Give the extent of all uninfected red blood cells.
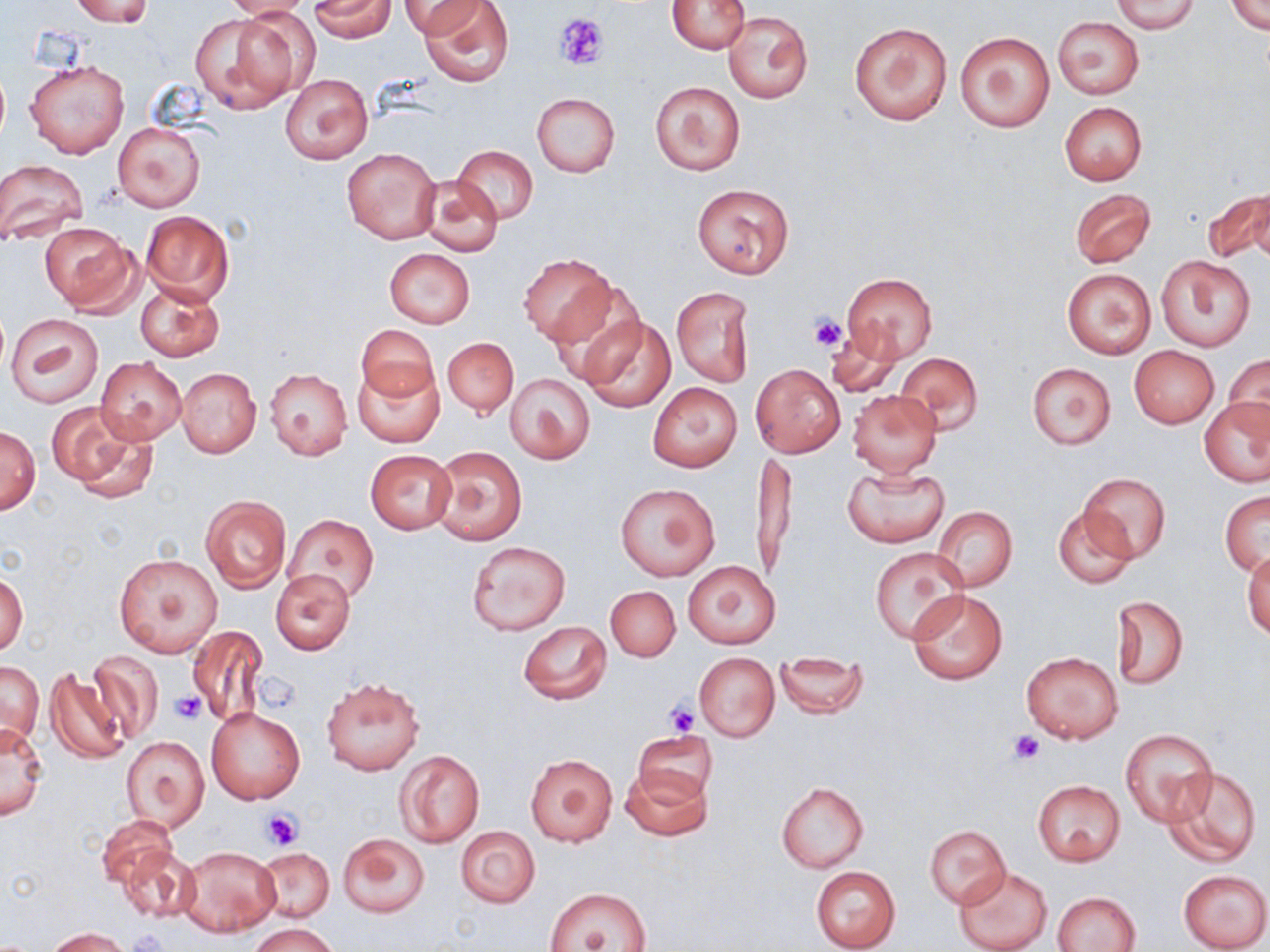

Approximate bounding boxes as (x1, y1, x2, y2) in pixels.
Uninfected red blood cells: (70, 0, 155, 26), (221, 0, 314, 20), (308, 0, 396, 41), (400, 0, 488, 38), (1111, 0, 1200, 33), (420, 1, 515, 87), (667, 1, 749, 53), (1227, 1, 1269, 35), (724, 11, 812, 104), (192, 13, 301, 113), (1052, 16, 1144, 99), (850, 23, 952, 126), (954, 31, 1057, 133), (25, 58, 129, 159), (281, 73, 372, 163), (650, 80, 745, 176), (531, 92, 620, 176), (1059, 101, 1146, 185), (113, 121, 205, 213), (455, 145, 537, 224), (342, 146, 441, 244), (0, 159, 89, 246), (416, 175, 502, 258), (692, 182, 793, 279), (1203, 187, 1270, 265), (1071, 188, 1156, 268), (140, 210, 236, 306), (39, 224, 141, 315), (384, 248, 475, 326), (519, 254, 613, 343), (1157, 255, 1255, 352), (1061, 267, 1157, 359), (842, 273, 938, 363), (548, 278, 648, 385), (135, 282, 224, 361), (670, 287, 756, 387), (5, 313, 104, 407), (578, 315, 675, 414), (356, 324, 438, 402), (825, 326, 902, 401), (443, 338, 517, 417), (1130, 345, 1219, 429), (894, 352, 983, 435), (1226, 354, 1269, 436), (94, 357, 186, 444), (355, 363, 442, 447), (1027, 363, 1116, 449), (752, 365, 845, 457), (176, 368, 261, 457), (265, 368, 352, 460), (504, 373, 595, 463), (649, 383, 741, 472), (848, 389, 942, 476), (1200, 398, 1269, 486), (46, 401, 158, 501), (0, 427, 40, 514), (432, 446, 526, 546), (751, 449, 797, 587), (366, 450, 455, 533), (843, 465, 949, 548), (1077, 473, 1170, 563), (615, 482, 721, 581), (1220, 490, 1269, 575), (201, 495, 291, 592), (1052, 504, 1137, 589), (931, 506, 1017, 592), (286, 514, 377, 603), (465, 541, 570, 635), (869, 546, 968, 643), (1243, 551, 1270, 641), (113, 553, 222, 657), (684, 561, 779, 648), (272, 569, 356, 655), (1, 570, 28, 656), (605, 585, 679, 662), (907, 587, 1008, 685), (1112, 594, 1189, 691), (517, 620, 612, 704), (187, 625, 267, 727), (87, 650, 163, 745), (1021, 651, 1123, 744), (775, 652, 868, 719), (695, 653, 779, 741), (1, 661, 43, 748), (44, 668, 132, 765), (322, 678, 424, 775), (206, 707, 306, 804), (1, 722, 48, 820), (1119, 728, 1220, 828), (633, 730, 719, 806), (121, 736, 209, 832), (394, 748, 486, 848), (525, 752, 617, 847), (620, 763, 712, 841), (1164, 767, 1261, 866), (1032, 779, 1125, 867), (777, 783, 868, 872), (96, 815, 175, 891), (925, 825, 1010, 909), (455, 826, 540, 907), (338, 832, 430, 918), (118, 846, 201, 925), (179, 846, 282, 936), (255, 847, 334, 923), (954, 866, 1052, 952), (810, 867, 901, 952), (1177, 869, 1269, 952), (543, 886, 652, 952), (1053, 891, 1141, 952), (247, 921, 340, 951), (45, 927, 131, 951).

slide_level_diagnosis: no evidence of blood parasites
preparation: thin blood film
magnification: 1000x
image_size: 1270×952 pixels
modality: optical microscopy
platelet_locations: 'approximate bounding boxes as (x1, y1, x2, y2) in pixels: (554, 13, 610, 70), (809, 314, 848, 354), (258, 670, 302, 713), (170, 693, 207, 725), (663, 700, 701, 736), (1009, 733, 1045, 765), (261, 809, 303, 850), (128, 928, 166, 952)'
field_of_view: single
stain: May-Grünwald-Giemsa